Look for Plasmodium parasites.
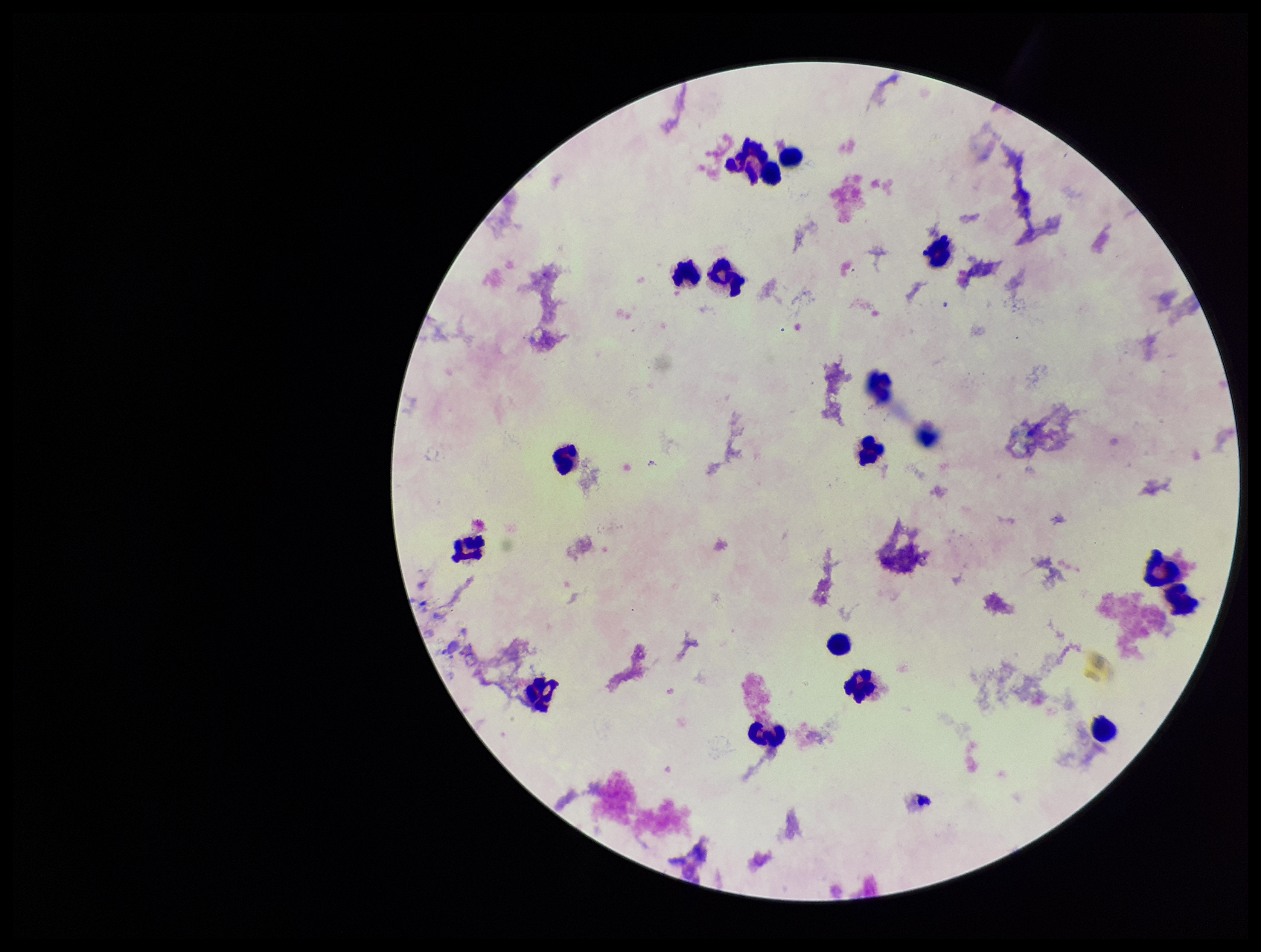

None seen.

One field from this slide. Image is 1261×952 pixels. Parasite count: 0. Patient malaria status: negative. Smartphone photograph taken through the eyepiece of a microscope. Stained with Giemsa. Preparation: thick smear. Leukocyte count: 16.